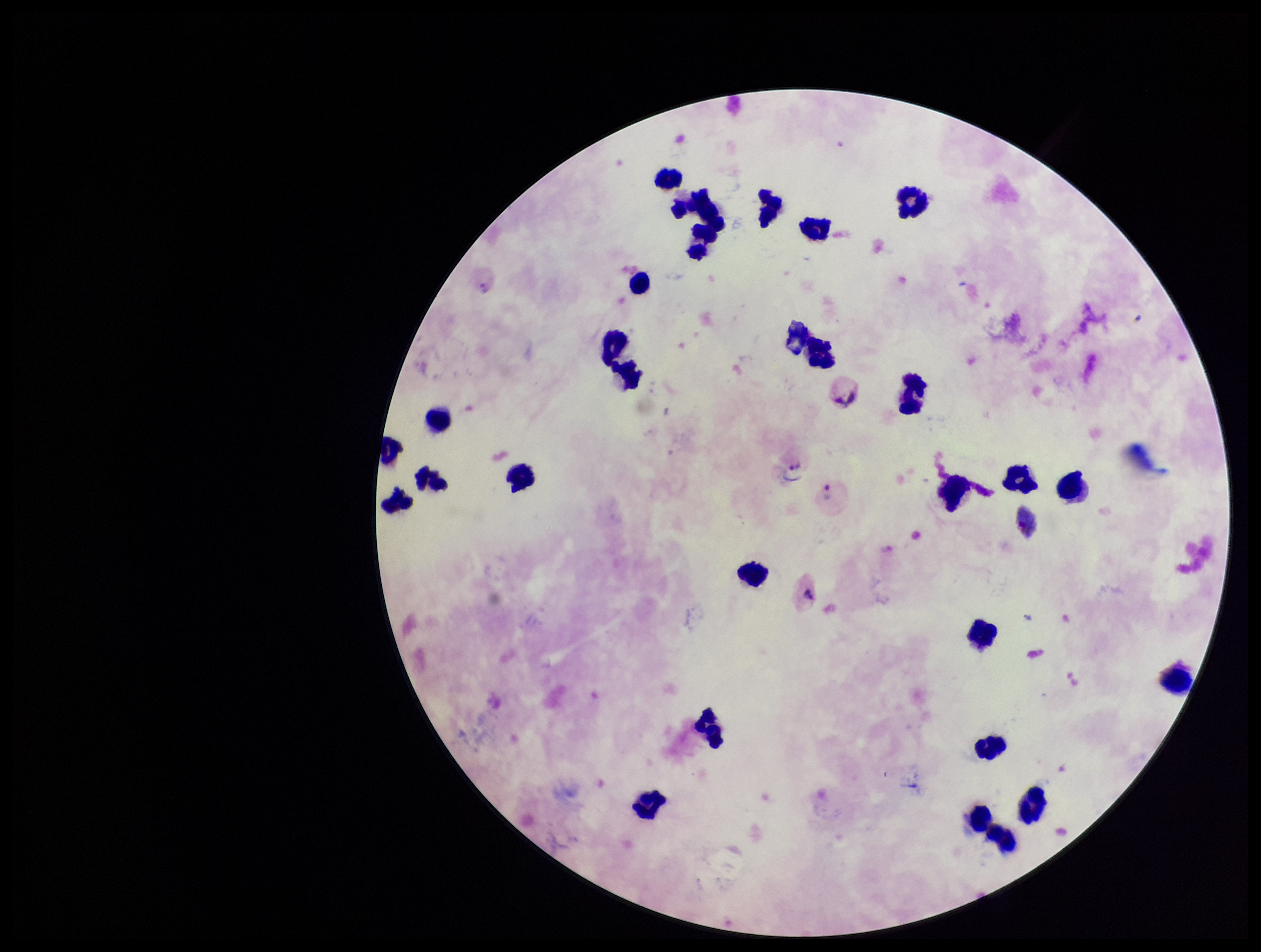
capture = smartphone photograph through the microscope eyepiece
image size = 1261×952 pixels
Plasmodium parasites = seen
stain = Giemsa
parasite count = 2
patient malaria status = positive
preparation = thick
species reported for this patient = Plasmodium vivax
leukocyte count = 30
field of view = single